Classify this cell by malaria status.
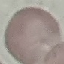

It is uninfected.

Giemsa-stained preparation. Automatically extracted cell patch, resized to 64 × 64 pixels. Thin blood smear. Acquired by smartphone through the microscope eyepiece.